Identify the cell.
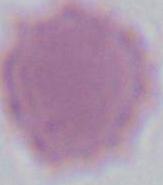

This is an erythrocyte.

Captured at 1000x magnification. Photomicrograph.